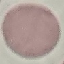

Malaria status: uninfected. Automatically extracted cell patch, resized to 64 × 64 pixels. Giemsa-stained preparation. Thin smear of blood. Acquired by smartphone through the microscope eyepiece.